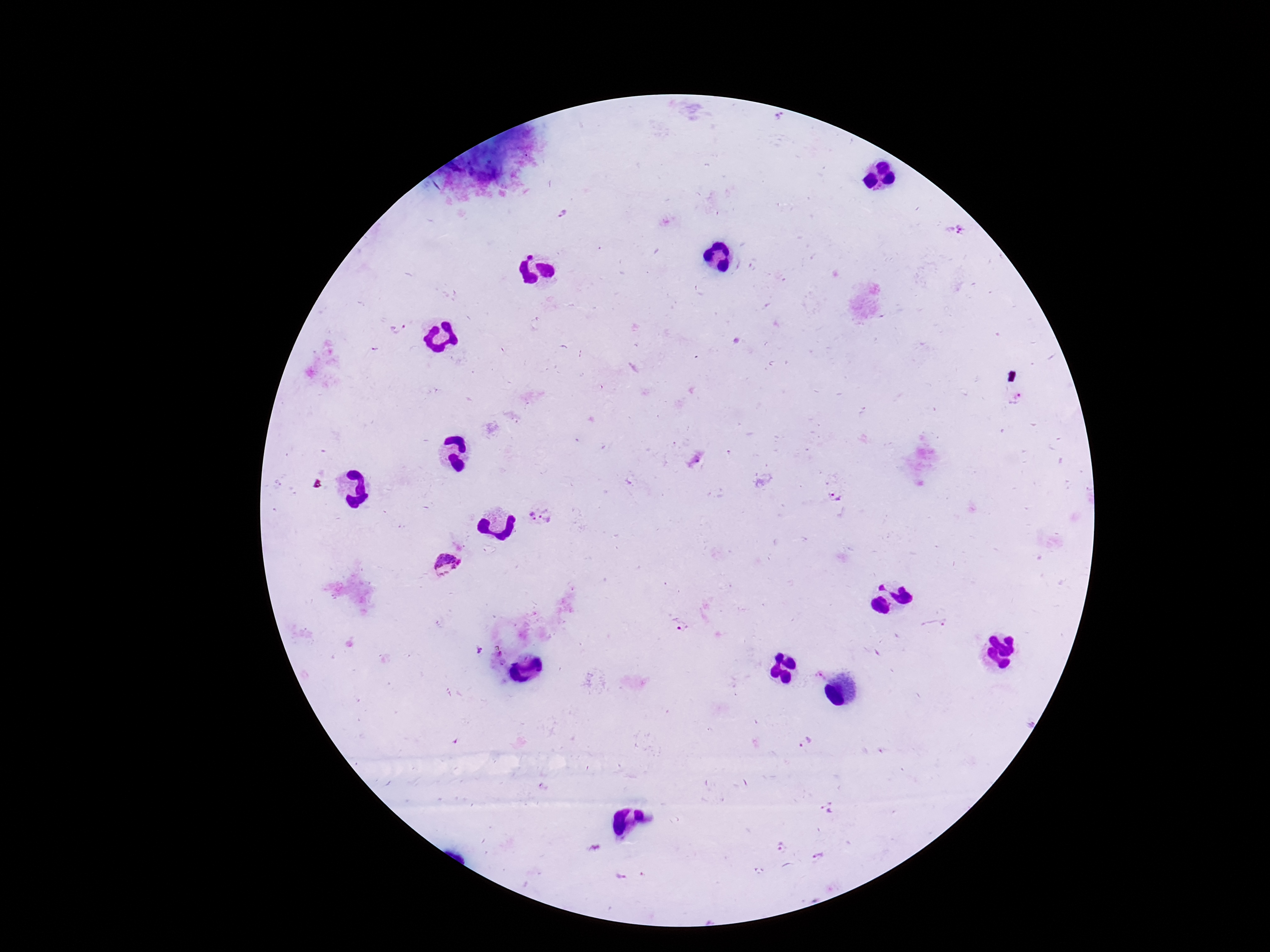

patient malaria status = positive
field of view = single
stain = Giemsa
preparation = thick blood film
Plasmodium parasite locations = approximate centers as {x, y} in pixels: {562, 214}, {961, 231}, {394, 331}, {837, 497}, {552, 513}, {531, 515}, {446, 562}, {684, 622}, {803, 743}, {829, 809}, {781, 845}, {817, 857}
magnification = 100x
image size = 1270×952 pixels
capture = smartphone camera through the microscope eyepiece